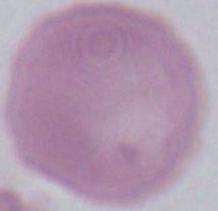
Summary:
  - Magnification: 1000x
  - Modality: micrograph
  - Identification: erythrocyte